Outline each Plasmodium falciparum-infected red blood cell.
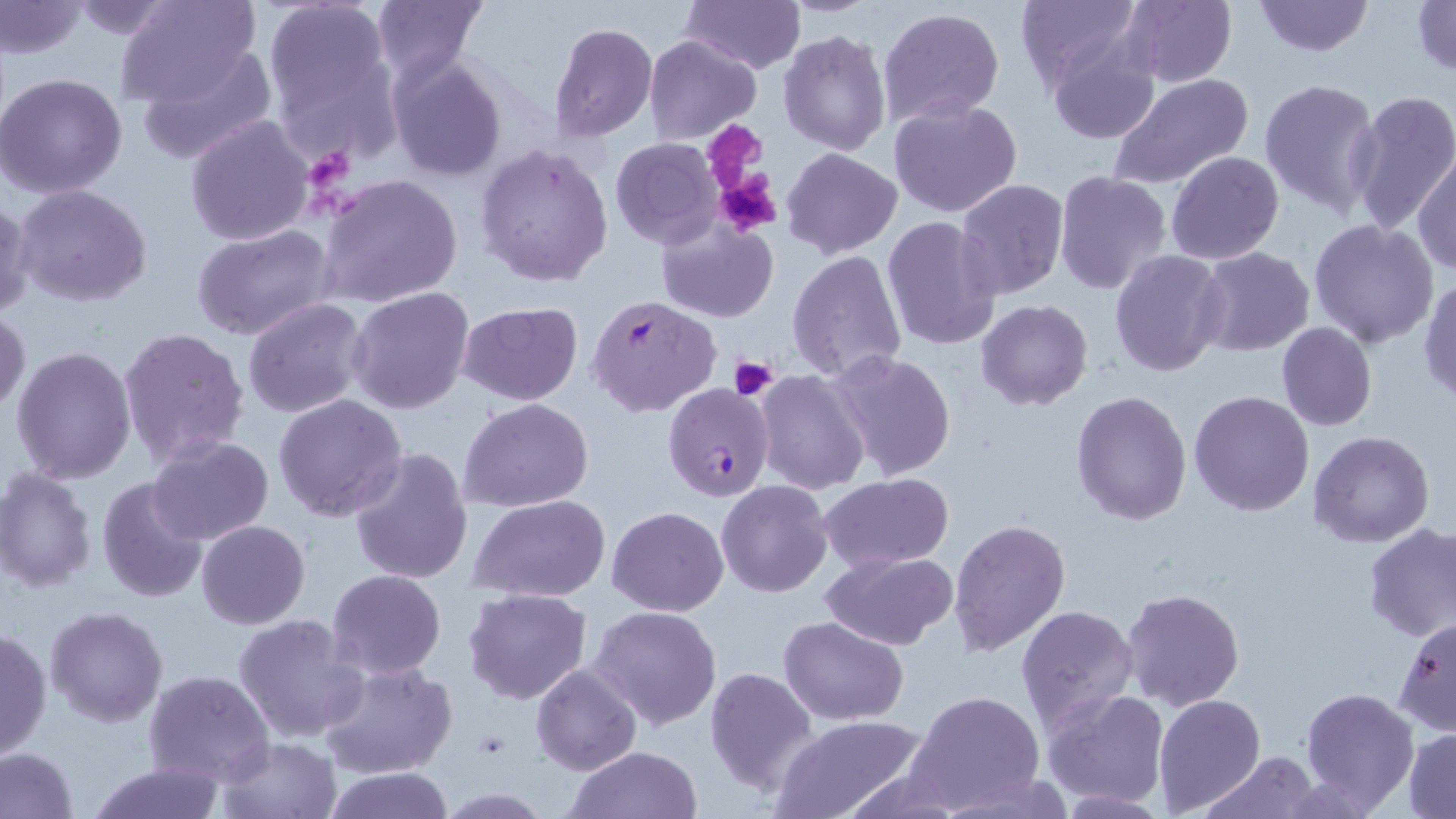

Approximate bounding boxes as (x1,y1)-(x2,y2) corner pairs in pixels.
Plasmodium falciparum-infected red blood cells: (586,295)-(722,418), (663,381)-(777,503).

slide-level diagnosis = Plasmodium falciparum
field of view = single
stain = May-Grünwald-Giemsa
uninfected red blood cell locations = approximate bounding boxes as (x1,y1)-(x2,y2) corner pairs in pixels: (113,0)-(264,110), (265,0)-(392,123), (370,0)-(487,84), (682,0)-(803,74), (1014,0)-(1146,95), (1251,0)-(1375,57), (1411,0)-(1456,77), (0,1)-(89,61), (61,1)-(191,40), (1119,1)-(1237,87), (877,8)-(1005,127), (549,22)-(657,142), (778,29)-(889,156), (644,35)-(760,143), (1045,35)-(1162,144), (137,42)-(279,164), (386,52)-(508,182), (1,71)-(130,197), (1108,72)-(1253,189), (1259,77)-(1382,218), (1346,90)-(1456,237), (886,98)-(1025,219), (184,114)-(314,246), (610,138)-(724,250), (475,143)-(614,289), (781,147)-(902,259), (1166,151)-(1284,264), (1415,151)-(1456,276), (317,171)-(463,309), (1054,171)-(1171,293), (956,179)-(1069,299), (13,184)-(152,308), (0,196)-(34,319), (656,214)-(777,322), (881,215)-(1003,352), (1309,220)-(1440,349), (191,224)-(336,343), (1195,247)-(1314,357), (786,248)-(908,384), (1110,249)-(1228,377), (1420,278)-(1456,405), (346,287)-(475,413), (242,298)-(369,419), (975,299)-(1093,410), (457,302)-(583,403), (0,307)-(30,417), (1276,323)-(1377,432), (118,327)-(251,471), (9,345)-(137,485), (825,349)-(956,481), (754,371)-(870,495), (1072,389)-(1192,524), (1189,389)-(1314,516), (273,393)-(407,521), (460,398)-(594,513), (1308,430)-(1436,548), (147,436)-(274,545), (348,446)-(475,583), (0,468)-(97,592), (818,473)-(953,573), (97,477)-(209,606), (716,480)-(832,598), (469,496)-(608,603), (607,505)-(728,616), (950,518)-(1070,656), (196,520)-(309,629), (1363,522)-(1456,641), (823,551)-(958,650), (327,569)-(445,679), (464,588)-(592,705), (1123,588)-(1245,712), (1016,604)-(1139,734), (586,605)-(724,732), (45,606)-(168,728), (235,613)-(369,743), (1395,614)-(1456,736), (779,615)-(910,726), (0,627)-(51,764), (319,660)-(457,779), (531,663)-(641,776), (703,666)-(818,797), (143,669)-(274,786), (1299,685)-(1418,814), (1041,687)-(1169,807), (907,689)-(1043,811), (1154,693)-(1266,813), (772,714)-(926,819), (1404,729)-(1456,816), (216,736)-(341,817), (0,747)-(81,819), (566,747)-(701,819), (1201,752)-(1317,819), (85,761)-(229,818), (320,767)-(453,819)
modality = light microscopy
preparation = thin blood smear
platelet locations = approximate bounding boxes as (x1,y1)-(x2,y2) corner pairs in pixels: (708,121)-(761,182), (311,146)-(357,194), (712,169)-(782,236), (729,355)-(778,401)
image size = 1456×819 pixels
magnification = 1000x